Comment on the morphology of the erythrocytes.
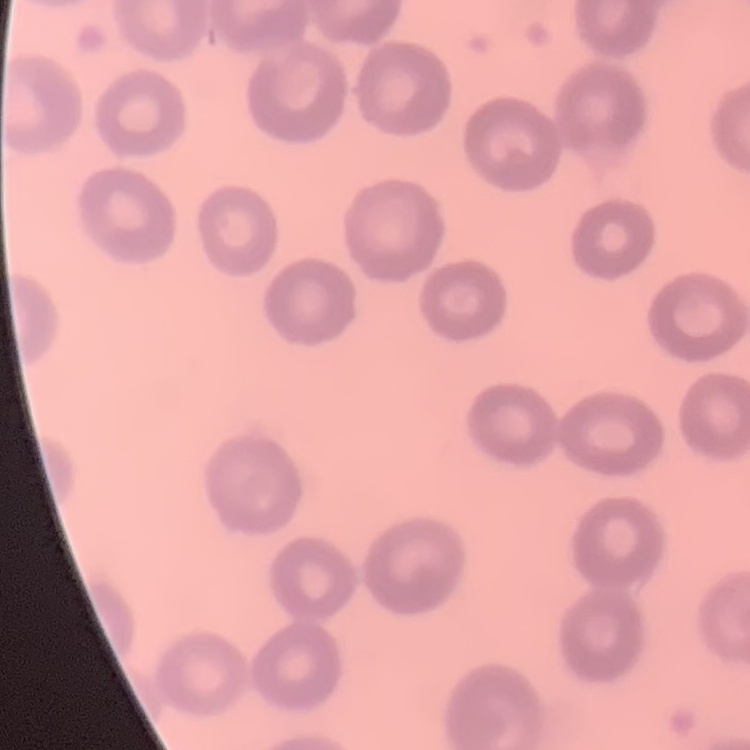
They show no rouleaux formation.

Thin blood film. Field's or Giemsa stain. One tile cut from a larger photomicrograph.